Identify the blood parasite species.
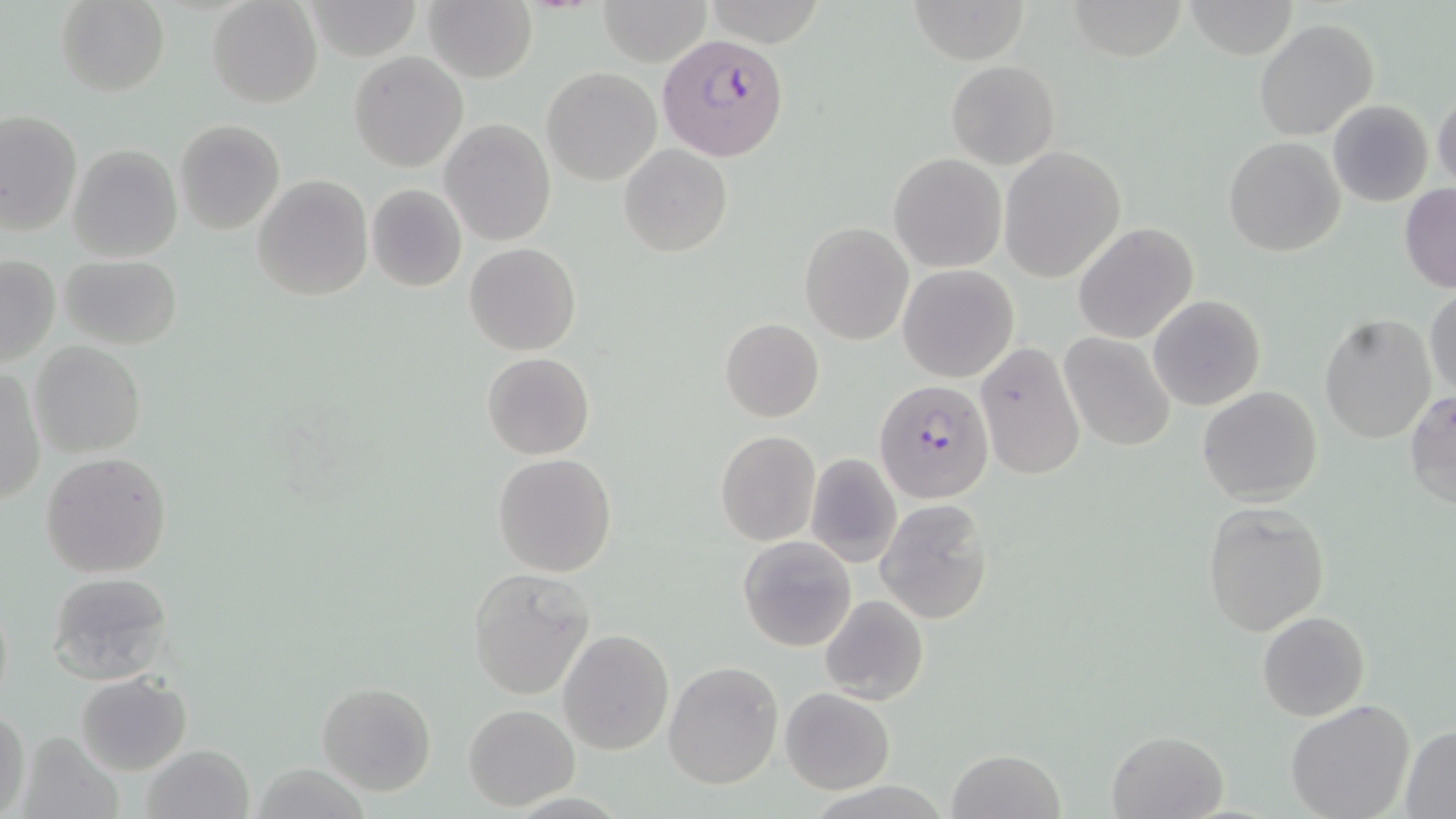

Plasmodium falciparum.

{
  "preparation": "thin blood smear",
  "field_of_view": "single",
  "stain": "May-Grünwald-Giemsa",
  "image_size": "1456×819 pixels",
  "modality": "light microscopy",
  "plasmodium_falciparum_infected_red_blood_cell_locations": "approximate bounding boxes as named x1/y1/x2/y2 corners in pixels: (x1=655, y1=31, x2=788, y2=164), (x1=873, y1=379, x2=994, y2=504)",
  "uninfected_red_blood_cell_locations": "approximate bounding boxes as named x1/y1/x2/y2 corners in pixels: (x1=55, y1=0, x2=170, y2=96), (x1=207, y1=0, x2=323, y2=108), (x1=307, y1=0, x2=420, y2=59), (x1=596, y1=0, x2=713, y2=66), (x1=914, y1=0, x2=1030, y2=64), (x1=425, y1=1, x2=536, y2=82), (x1=1184, y1=1, x2=1298, y2=59), (x1=701, y1=2, x2=827, y2=45), (x1=1253, y1=18, x2=1379, y2=140), (x1=349, y1=51, x2=467, y2=171), (x1=945, y1=60, x2=1061, y2=170), (x1=541, y1=66, x2=662, y2=185), (x1=1432, y1=89, x2=1456, y2=192), (x1=1326, y1=99, x2=1435, y2=205), (x1=0, y1=109, x2=83, y2=238), (x1=440, y1=119, x2=555, y2=246), (x1=174, y1=120, x2=286, y2=236), (x1=1223, y1=136, x2=1344, y2=256), (x1=67, y1=142, x2=182, y2=262), (x1=618, y1=143, x2=733, y2=257), (x1=998, y1=146, x2=1126, y2=282), (x1=889, y1=153, x2=1006, y2=273), (x1=252, y1=174, x2=375, y2=302), (x1=365, y1=184, x2=467, y2=292), (x1=1399, y1=185, x2=1456, y2=292), (x1=800, y1=222, x2=912, y2=344), (x1=1073, y1=222, x2=1199, y2=346), (x1=464, y1=242, x2=580, y2=355), (x1=58, y1=254, x2=183, y2=349), (x1=1, y1=255, x2=60, y2=368), (x1=897, y1=264, x2=1019, y2=382), (x1=1425, y1=288, x2=1455, y2=403), (x1=1148, y1=295, x2=1266, y2=410), (x1=1319, y1=315, x2=1437, y2=444), (x1=719, y1=318, x2=824, y2=423), (x1=1060, y1=332, x2=1178, y2=453), (x1=31, y1=341, x2=146, y2=458), (x1=975, y1=342, x2=1085, y2=480), (x1=482, y1=352, x2=595, y2=460), (x1=0, y1=364, x2=46, y2=505), (x1=1197, y1=386, x2=1324, y2=505), (x1=1406, y1=391, x2=1456, y2=510), (x1=715, y1=429, x2=821, y2=547), (x1=40, y1=451, x2=171, y2=579), (x1=492, y1=452, x2=619, y2=577), (x1=803, y1=452, x2=903, y2=568), (x1=875, y1=499, x2=992, y2=623), (x1=1200, y1=502, x2=1329, y2=634), (x1=738, y1=534, x2=857, y2=653), (x1=466, y1=567, x2=595, y2=699), (x1=48, y1=570, x2=173, y2=683), (x1=1, y1=590, x2=14, y2=716), (x1=818, y1=594, x2=929, y2=706), (x1=1257, y1=611, x2=1369, y2=721), (x1=556, y1=628, x2=674, y2=756), (x1=662, y1=660, x2=783, y2=789), (x1=76, y1=672, x2=192, y2=776), (x1=316, y1=682, x2=436, y2=796), (x1=779, y1=686, x2=896, y2=795), (x1=1285, y1=700, x2=1414, y2=819), (x1=463, y1=704, x2=580, y2=809), (x1=1, y1=709, x2=31, y2=816), (x1=1400, y1=727, x2=1456, y2=816), (x1=1106, y1=728, x2=1229, y2=819), (x1=17, y1=731, x2=121, y2=819), (x1=140, y1=744, x2=254, y2=819), (x1=945, y1=749, x2=1066, y2=819)",
  "magnification": "1000x"
}